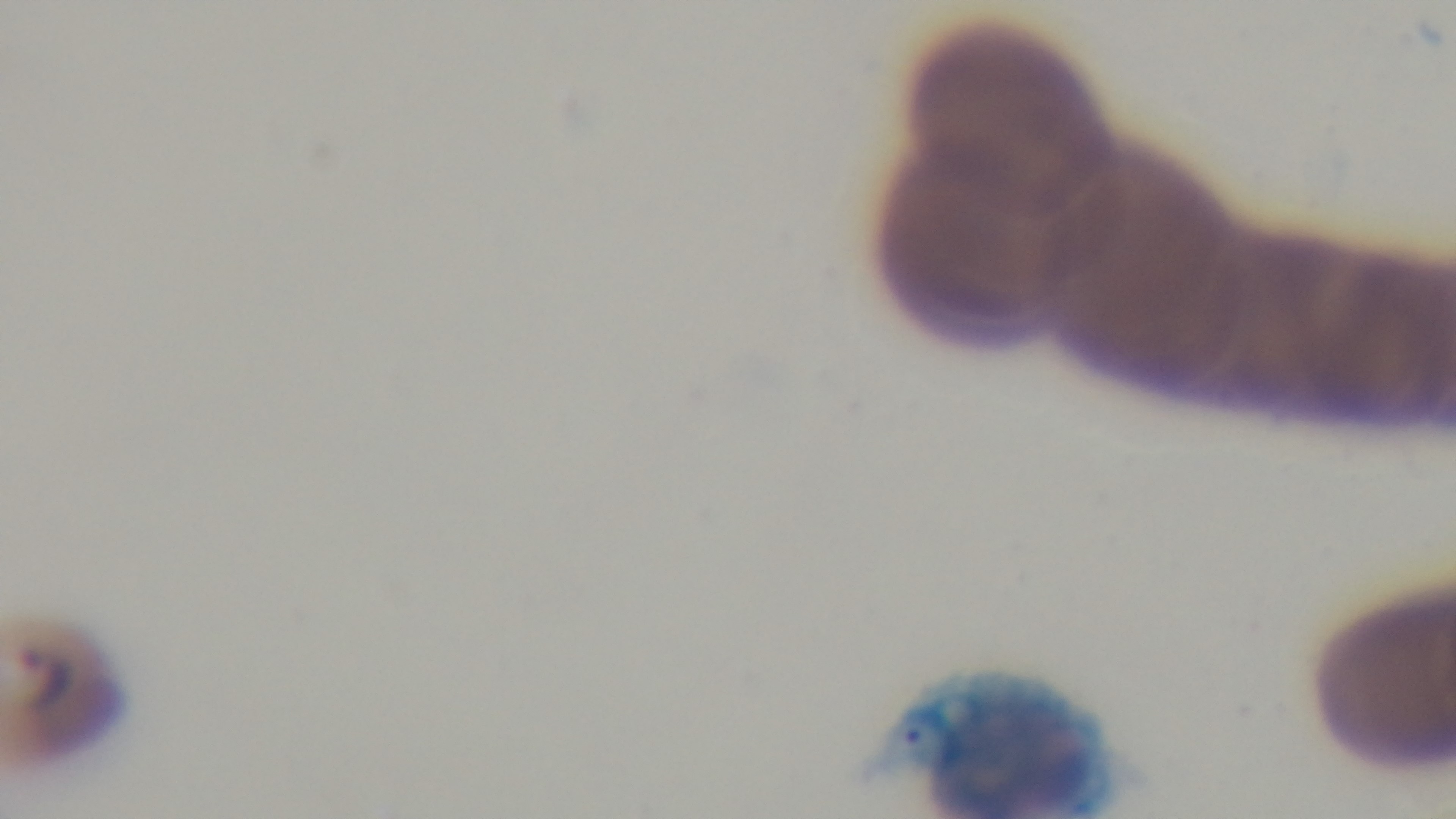 Preparation: thin smear. 100x oil-immersion objective. Giemsa stain. Captured with a mounted 4K digital camera. Light microscopy. One field from the slide. Malaria status: infected.